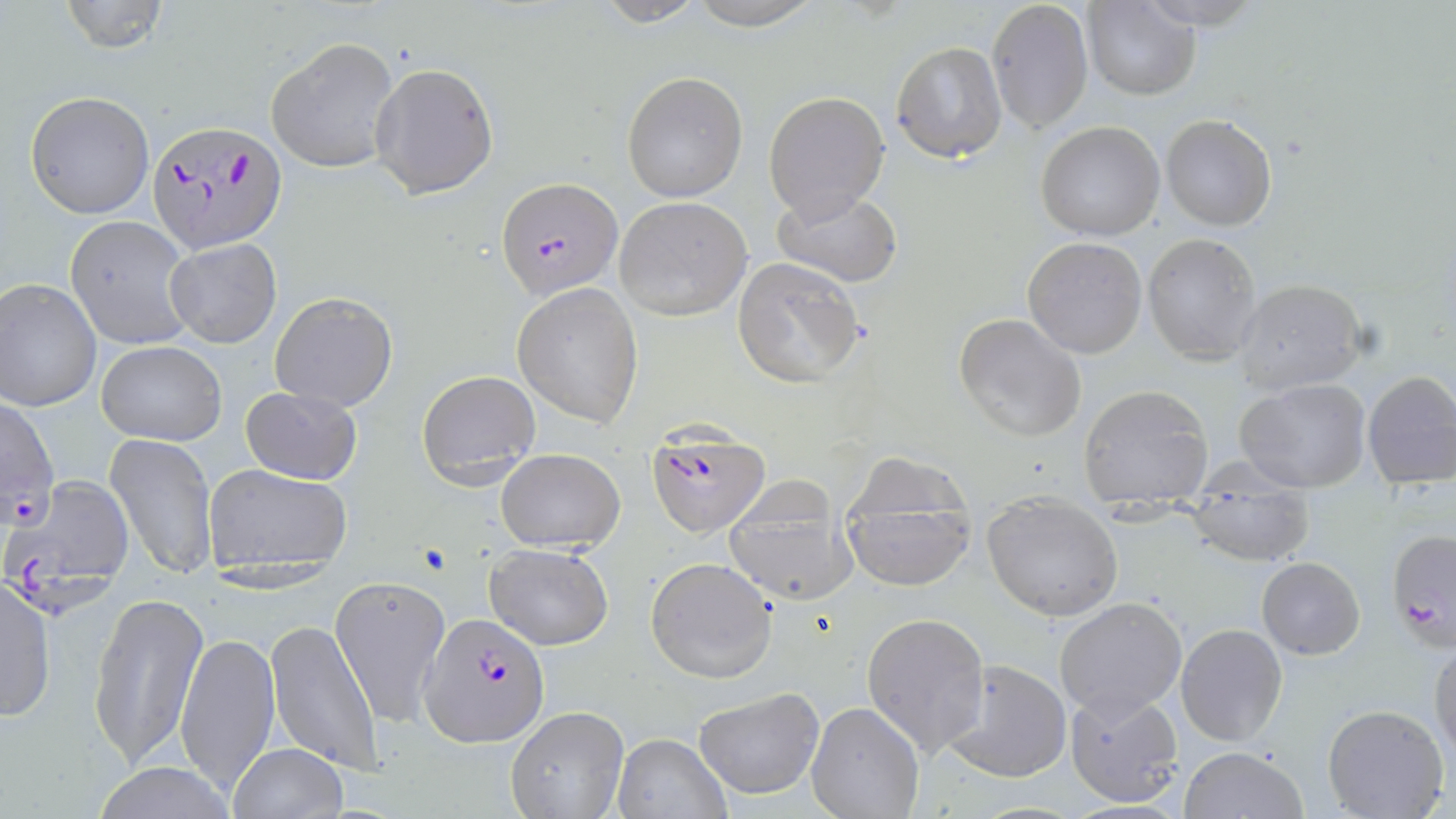
Summary:
  - Coordinate format: approximate bounding boxes as [x1, y1, x2, y2] in pixels
  - Uninfected red blood cell locations: [58, 0, 169, 54], [586, 0, 712, 26], [682, 0, 827, 29], [987, 1, 1092, 133], [1084, 2, 1198, 99], [267, 35, 400, 174], [891, 40, 1007, 164], [370, 60, 499, 198], [622, 70, 748, 202], [763, 90, 891, 220], [25, 91, 154, 219], [1161, 114, 1277, 231], [1036, 120, 1165, 241], [771, 187, 903, 289], [614, 196, 751, 320], [65, 217, 193, 348], [1142, 233, 1264, 365], [1023, 236, 1147, 358], [165, 238, 282, 348], [732, 255, 865, 389], [0, 279, 101, 412], [1233, 279, 1368, 394], [512, 282, 645, 428], [270, 291, 398, 413], [954, 311, 1088, 444], [96, 341, 227, 446], [415, 369, 542, 488], [1361, 370, 1456, 487], [1234, 379, 1371, 492], [1078, 383, 1213, 503], [241, 385, 363, 485], [105, 432, 216, 583], [496, 449, 625, 553], [836, 453, 981, 594], [203, 462, 354, 583], [723, 476, 855, 607], [1182, 483, 1316, 569], [981, 495, 1124, 620], [1396, 530, 1456, 648], [485, 542, 614, 650], [646, 556, 778, 685], [1256, 556, 1366, 659], [332, 575, 452, 730], [1, 576, 56, 722], [88, 589, 209, 771], [1054, 597, 1187, 718], [861, 612, 990, 758], [266, 618, 383, 774], [1175, 624, 1289, 747], [176, 627, 281, 797], [1431, 640, 1456, 765], [944, 660, 1073, 784], [694, 686, 824, 799], [1062, 687, 1184, 807], [806, 701, 925, 818], [1322, 703, 1450, 819], [504, 708, 630, 819], [612, 732, 730, 818], [225, 743, 349, 819], [1179, 746, 1310, 819], [93, 761, 235, 818]
  - Plasmodium falciparum-infected red blood cell locations: [146, 118, 288, 255], [498, 179, 623, 300], [0, 398, 59, 521], [648, 422, 769, 539], [3, 476, 137, 615], [418, 613, 549, 747]
  - Slide-level diagnosis: Plasmodium falciparum
  - Stain: May-Grünwald-Giemsa
  - Modality: optical microscopy
  - Magnification: 1000x
  - Image size: 1456×819 pixels
  - Field of view: single
  - Preparation: thin blood smear